Locate and identify every blood parasite.
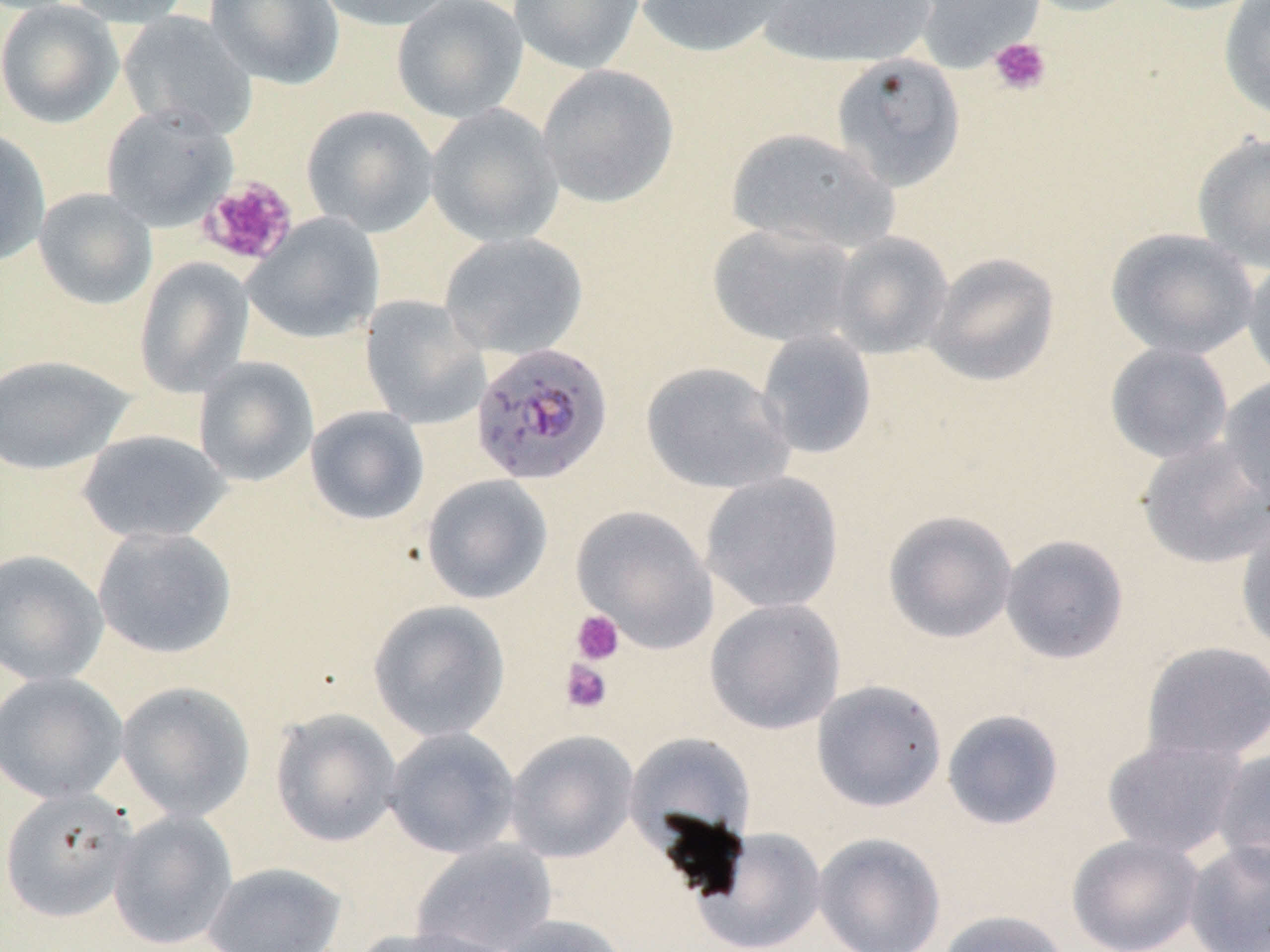
Approximate bounding boxes as named x1/y1/x2/y2 corners in pixels.
Plasmodium falciparum-infected red blood cells: (x1=470, y1=342, x2=614, y2=486).
No Plasmodium ovale, Plasmodium malariae, Plasmodium vivax, Babesia divergens, or Trypanosoma brucei observed.

Platelet locations (subset): (x1=988, y1=37, x2=1052, y2=96), (x1=199, y1=176, x2=298, y2=267), (x1=571, y1=610, x2=624, y2=665), (x1=559, y1=659, x2=612, y2=714). Uninfected red blood cell locations (subset): (x1=0, y1=0, x2=124, y2=129), (x1=58, y1=0, x2=195, y2=27), (x1=205, y1=0, x2=344, y2=89), (x1=313, y1=0, x2=461, y2=31), (x1=391, y1=0, x2=528, y2=123), (x1=508, y1=0, x2=645, y2=74), (x1=635, y1=0, x2=797, y2=59), (x1=759, y1=0, x2=939, y2=68), (x1=912, y1=0, x2=1044, y2=72), (x1=1018, y1=0, x2=1147, y2=17), (x1=1135, y1=0, x2=1264, y2=16), (x1=1218, y1=0, x2=1270, y2=125), (x1=118, y1=11, x2=258, y2=141), (x1=830, y1=52, x2=966, y2=191), (x1=537, y1=65, x2=679, y2=208), (x1=301, y1=104, x2=438, y2=237), (x1=425, y1=104, x2=564, y2=248), (x1=0, y1=127, x2=51, y2=267), (x1=725, y1=127, x2=899, y2=255), (x1=1192, y1=133, x2=1270, y2=273), (x1=33, y1=188, x2=158, y2=310), (x1=243, y1=212, x2=384, y2=345), (x1=706, y1=221, x2=860, y2=348), (x1=1105, y1=227, x2=1260, y2=360), (x1=829, y1=231, x2=954, y2=360), (x1=439, y1=232, x2=587, y2=359), (x1=924, y1=252, x2=1060, y2=387), (x1=1242, y1=255, x2=1270, y2=389), (x1=133, y1=257, x2=255, y2=398), (x1=360, y1=295, x2=490, y2=429), (x1=755, y1=330, x2=877, y2=460), (x1=1105, y1=342, x2=1234, y2=464), (x1=0, y1=354, x2=135, y2=476), (x1=193, y1=357, x2=319, y2=487), (x1=640, y1=361, x2=795, y2=495), (x1=1217, y1=376, x2=1270, y2=511), (x1=305, y1=406, x2=430, y2=525), (x1=76, y1=429, x2=231, y2=544), (x1=1136, y1=436, x2=1269, y2=569), (x1=700, y1=472, x2=844, y2=614), (x1=421, y1=474, x2=553, y2=604), (x1=571, y1=505, x2=719, y2=654), (x1=883, y1=509, x2=1017, y2=644), (x1=1236, y1=521, x2=1270, y2=655), (x1=92, y1=525, x2=237, y2=660), (x1=1000, y1=534, x2=1130, y2=664), (x1=0, y1=549, x2=109, y2=687), (x1=368, y1=599, x2=510, y2=742), (x1=704, y1=599, x2=846, y2=734), (x1=1140, y1=641, x2=1270, y2=764), (x1=0, y1=671, x2=129, y2=805), (x1=811, y1=679, x2=947, y2=812), (x1=115, y1=681, x2=255, y2=822), (x1=270, y1=708, x2=402, y2=847), (x1=941, y1=709, x2=1065, y2=830), (x1=383, y1=726, x2=521, y2=858), (x1=504, y1=730, x2=639, y2=863), (x1=624, y1=731, x2=756, y2=856), (x1=1101, y1=735, x2=1250, y2=860), (x1=1212, y1=747, x2=1270, y2=878), (x1=0, y1=787, x2=138, y2=923), (x1=108, y1=809, x2=238, y2=950), (x1=692, y1=827, x2=827, y2=952), (x1=813, y1=832, x2=946, y2=952), (x1=1067, y1=834, x2=1203, y2=951), (x1=1183, y1=838, x2=1270, y2=952), (x1=412, y1=840, x2=557, y2=952), (x1=202, y1=861, x2=346, y2=952), (x1=936, y1=909, x2=1073, y2=952), (x1=493, y1=914, x2=633, y2=952), (x1=353, y1=925, x2=516, y2=952). Slide-level diagnosis: Plasmodium falciparum. May-Grünwald-Giemsa stain. Optical microscopy. Single field of view. Captured at 1000x magnification. Image is 1270×952 pixels. Thin blood film.